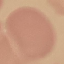
Summary:
  - Result: no malaria parasites seen
  - Capture: smartphone through the microscope eyepiece
  - Image type: cell patch, automatically extracted from a larger field of view and resized to 64 × 64 pixels
  - Stain: Giemsa
  - Preparation: thin blood smear